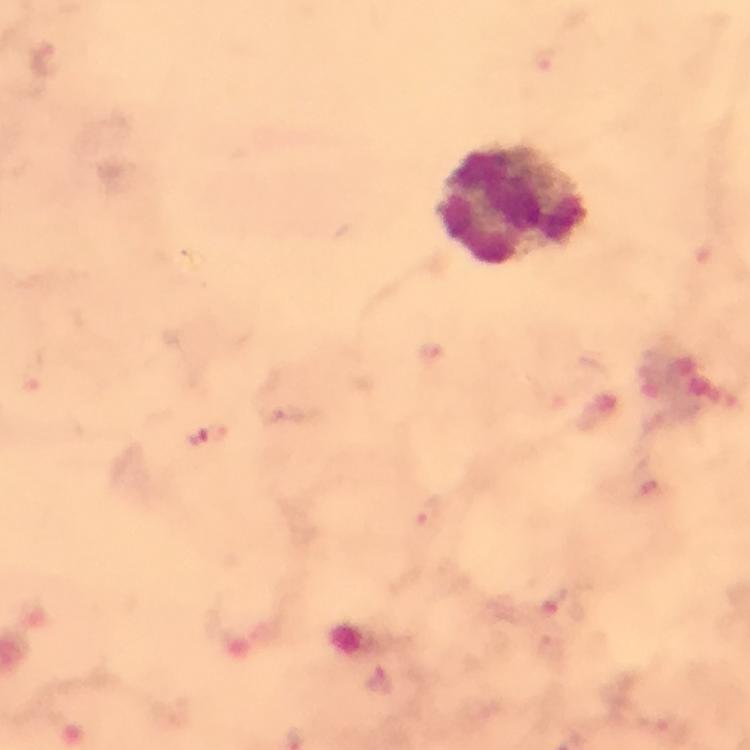 Approximate centers as [x, y] in pixels. Plasmodium parasite locations: [199, 439], [380, 679]. Leukocyte locations: [515, 204]. Cropped region of a single field of view. From a diagnostic examination for malaria. Thick smear. Giemsa-stained preparation. At 100x magnification. Photographed with a smartphone mounted on the microscope. Image is 750×750 pixels. Immersion oil applied.